State the preparation type.
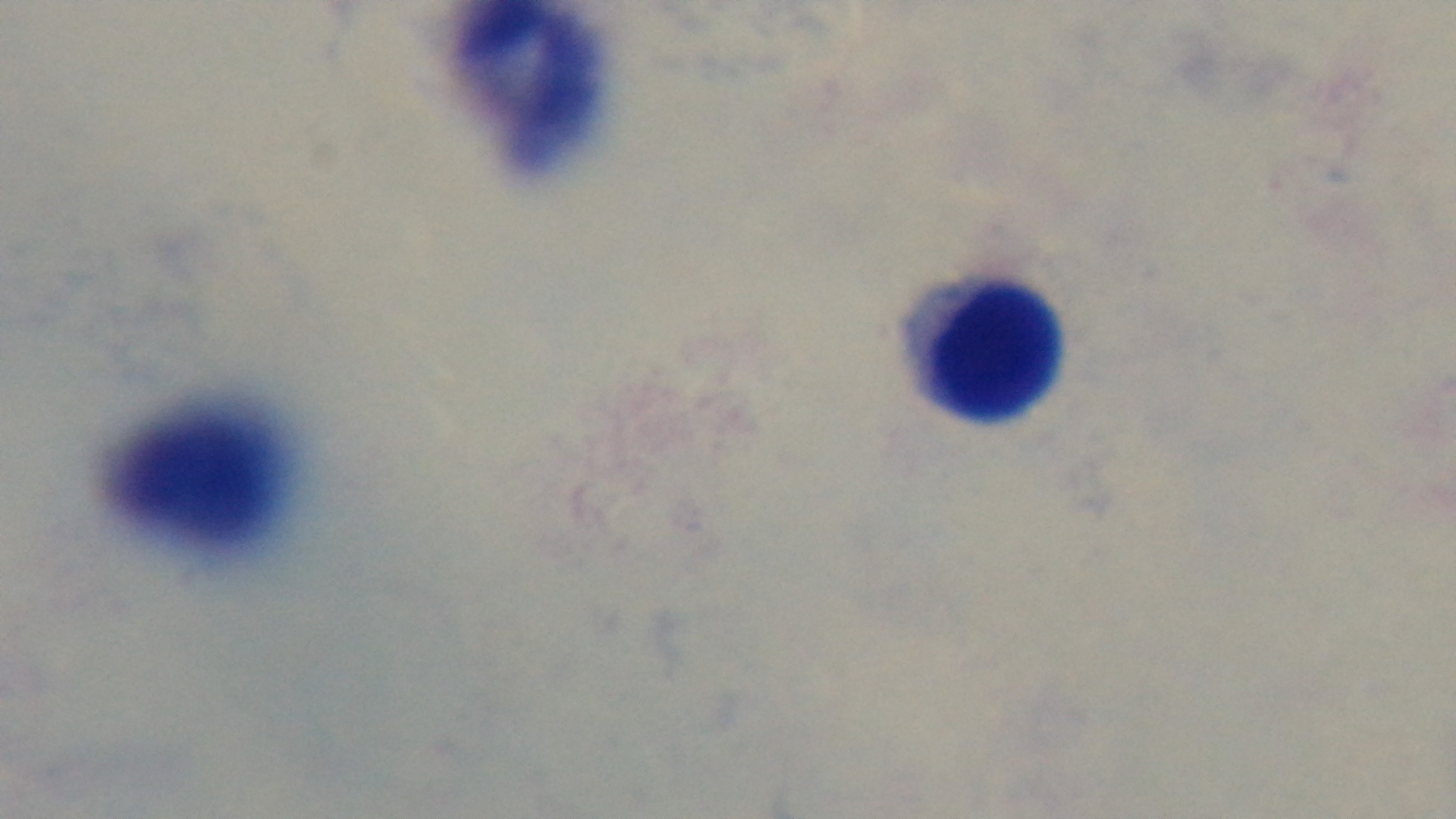

A thick smear.

{
  "stain": "Giemsa",
  "field_of_view": "one from the slide",
  "modality": "light microscopy",
  "objective": "100x oil immersion",
  "malaria_status": "negative",
  "capture": "mounted 4K digital camera"
}